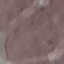 Result: no malaria parasites detected. Photographed with a smartphone camera at the microscope eyepiece. Giemsa stain. Cell patch, automatically extracted from a larger field of view and resized to 64 × 64 pixels. Thin smear of blood.